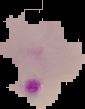
Cell region segmented out of the field of view; the surrounding area is masked to black. Image is 85×109 pixels. Malaria status: parasitized. From a thin blood smear.